Assess the morphology of the erythrocytes.
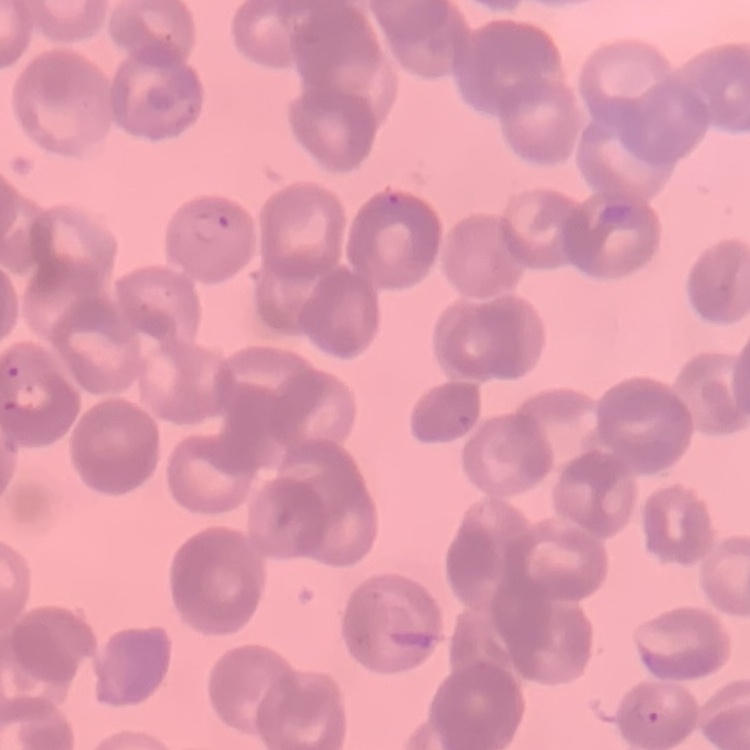

They show rouleaux formation.

image type = one tile cut from a larger photomicrograph
stain = Field's or Giemsa
preparation = thin blood film